Assess this cell for malaria.
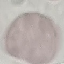
Uninfected.

Summary:
  - Image type: cell patch, automatically extracted from a larger field of view and resized to 64 × 64 pixels
  - Capture: smartphone camera at the microscope eyepiece
  - Preparation: thin blood smear
  - Stain: Giemsa